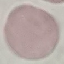

result = no malaria parasites seen
preparation = thin smear
capture = smartphone through the microscope eyepiece
stain = Giemsa
image type = cell patch, automatically extracted from a larger field of view and resized to 64 × 64 pixels